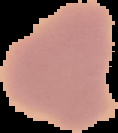 From a thin blood smear. Result: negative for malaria parasites. Image is 118×133 pixels. Cell region segmented out of the field of view; the surrounding area is masked to black.